Classify this cell by malaria status.
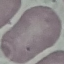

Uninfected.

image type = automatically extracted cell patch, resized to 64 × 64 pixels
stain = Giemsa
preparation = thin smear
capture = smartphone through the microscope eyepiece